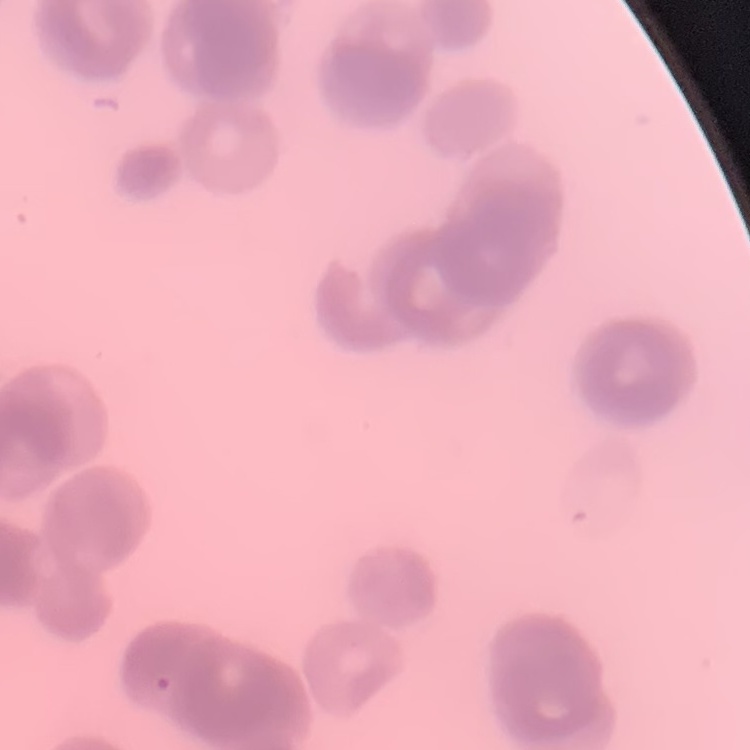
Summary:
  - Red blood cell morphology: rouleaux formation
  - Image type: one tile cut from a larger photomicrograph
  - Preparation: thin blood smear
  - Stain: Field's or Giemsa